Find the red blood cells and label each as P. falciparum-infected, uninfected, or of indeterminate infection status.
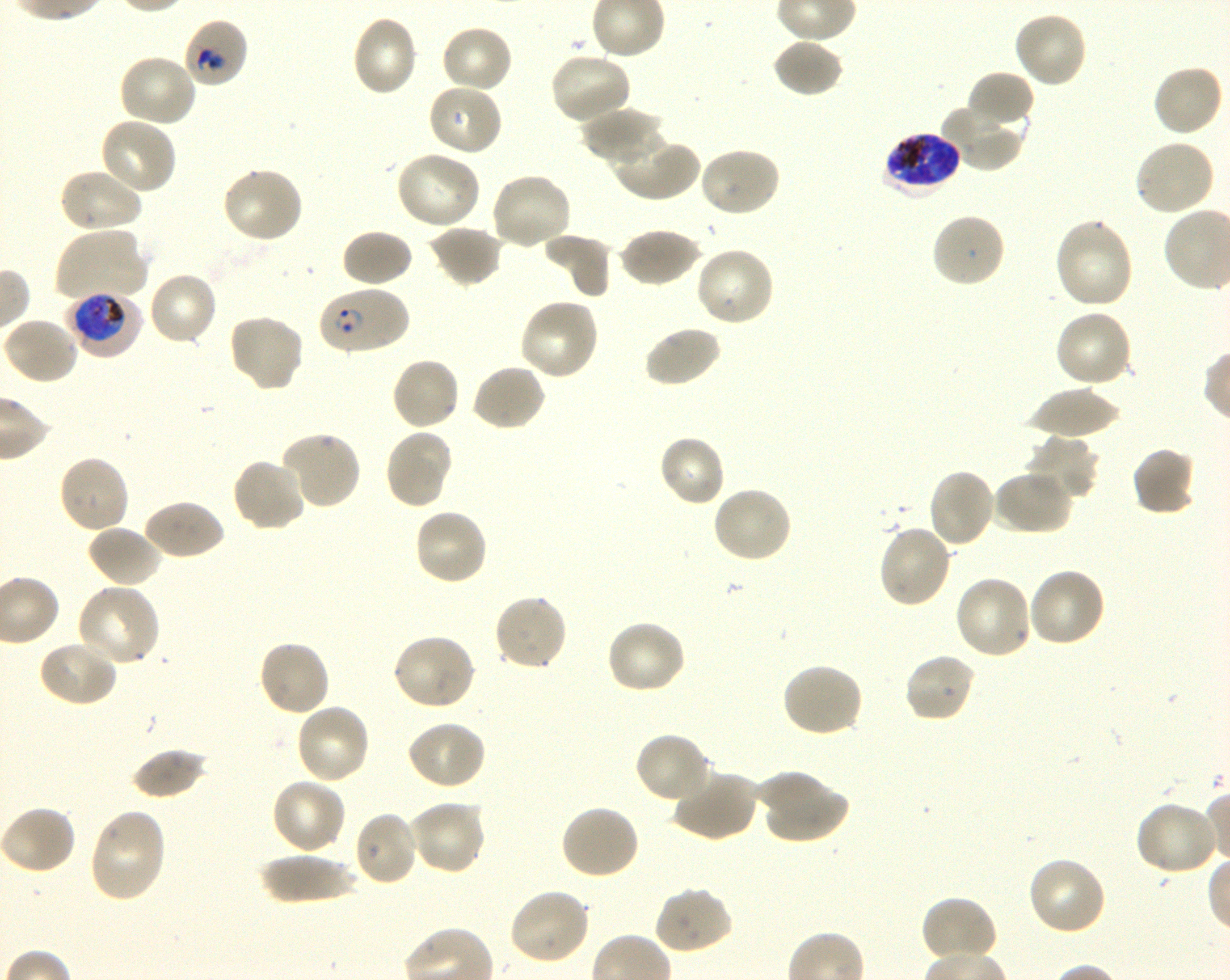
Approximate bounding boxes as (x1, y1, x2, y2) in pixels. Not every red blood cell is marked. A life-cycle stage — or a range of stages, where the recorded stages span more than one — follows each staged infected red blood cell.
Infected red blood cells: (883, 131, 961, 194) late trophozoite to late schizont; (318, 287, 408, 355) ring; (69, 291, 143, 359) early trophozoite to early schizont.
Red blood cells of indeterminate infection status: (181, 17, 249, 89).
Uninfected red blood cells: (1013, 10, 1088, 89), (350, 14, 420, 98), (440, 24, 514, 94), (772, 38, 845, 97), (548, 52, 633, 125), (117, 53, 198, 128), (1151, 64, 1226, 139), (965, 71, 1035, 131), (427, 83, 504, 157), (942, 104, 1026, 172), (581, 105, 665, 166), (99, 115, 178, 196), (609, 131, 699, 202), (1132, 138, 1215, 218), (698, 146, 781, 218), (394, 151, 482, 230), (57, 166, 143, 234), (220, 166, 305, 245), (489, 171, 573, 251), (931, 211, 1006, 289), (1053, 217, 1134, 311), (427, 224, 505, 288), (619, 226, 701, 288), (52, 228, 148, 302), (340, 229, 414, 288), (543, 232, 614, 300), (694, 245, 775, 328), (146, 271, 219, 347), (519, 297, 601, 382), (1053, 308, 1134, 389), (227, 312, 305, 393), (3, 317, 81, 386), (643, 325, 722, 389), (390, 357, 462, 432), (471, 363, 547, 432), (1024, 386, 1124, 438), (383, 428, 454, 509), (279, 431, 362, 511), (657, 434, 727, 508), (1024, 435, 1101, 507), (1131, 445, 1196, 516), (56, 454, 131, 535), (231, 457, 307, 532), (927, 467, 997, 550), (991, 470, 1072, 536), (711, 484, 794, 564), (142, 498, 225, 562), (412, 506, 489, 587), (86, 524, 163, 588), (876, 524, 954, 610), (1027, 567, 1107, 649), (953, 575, 1035, 661), (76, 583, 161, 667), (492, 593, 569, 671), (604, 620, 687, 696), (390, 632, 477, 710), (37, 639, 119, 707), (257, 639, 331, 718), (902, 652, 978, 725), (780, 662, 864, 739), (293, 702, 371, 786), (405, 719, 487, 791), (633, 731, 712, 805), (131, 747, 209, 800), (671, 770, 759, 843), (757, 770, 849, 845), (270, 777, 347, 856), (406, 799, 487, 876), (1133, 800, 1221, 876), (0, 804, 77, 876), (560, 804, 641, 881), (88, 808, 168, 903), (353, 811, 419, 887), (259, 853, 360, 904), (1026, 856, 1108, 938), (653, 885, 733, 955), (507, 887, 591, 965), (919, 896, 998, 966).

Summary:
  - Image size: 1230×980 pixels
  - Field of view: single
  - Objective: 100x, oil immersion, numerical aperture 1.30
  - Stain: Giemsa
  - Culture: shaking in-vitro P. falciparum strain 3D7
  - Donor blood group: O+
  - Preparation: thin blood smear